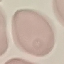

Malaria status: uninfected. Thin smear of blood. Acquired by smartphone through the microscope eyepiece. Cell patch, automatically extracted from a larger field of view and resized to 64 × 64 pixels. Giemsa-stained preparation.